Assess this cell for malaria.
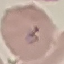

Parasitized.

Photographed with a smartphone camera at the microscope eyepiece. Giemsa-stained preparation. Thin smear of blood. Cell patch, automatically extracted from a larger field of view and resized to 64 × 64 pixels.